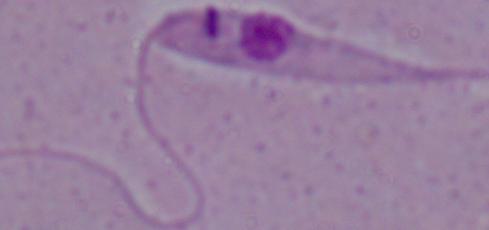
A Leishmania parasite is shown. Captured at 1000x magnification. Micrograph.